Report the malaria status of this cell.
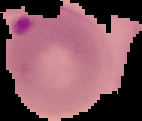
It is parasitized.

Image is 142×121 pixels. Cell region segmented out of the field of view; the surrounding area is masked to black. From a thin blood smear.